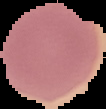

preparation = thin blood film
image size = 106×109 pixels
result = no malaria parasites detected
image type = cell region segmented out of the field of view; surrounding area masked to black